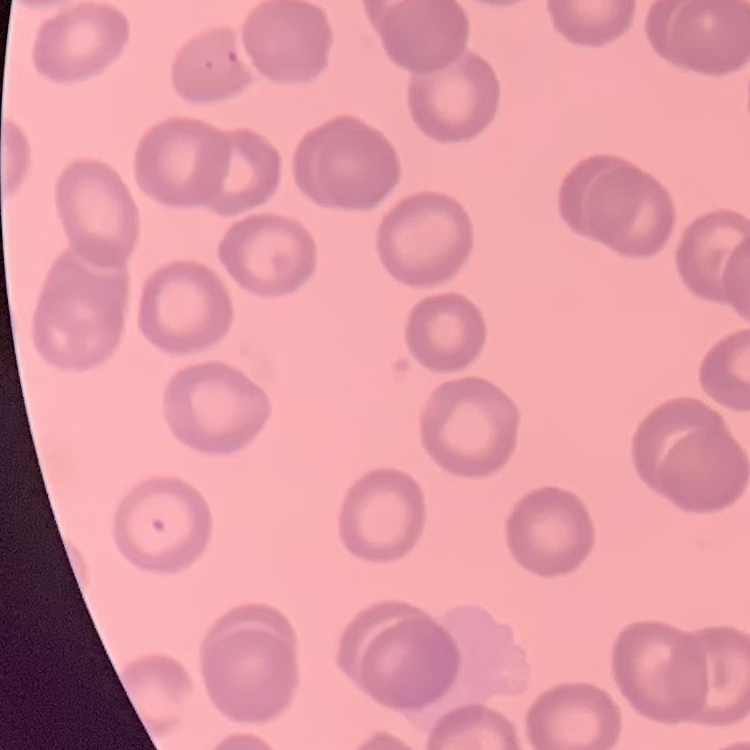

erythrocyte morphology = no rouleaux formation
image type = one tile cut from a larger photomicrograph
stain = Field's or Giemsa
preparation = thin blood film